Assess this cell for malaria.
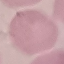
It is uninfected.

Thin smear of blood. Giemsa stain. Automatically extracted cell patch, resized to 64 × 64 pixels. Acquired by smartphone through the microscope eyepiece.